Report the malaria status of this cell.
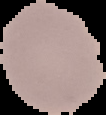
Uninfected.

preparation = thin blood film
image size = 106×115 pixels
image type = segmented cell region on a black background